Give the preparation type.
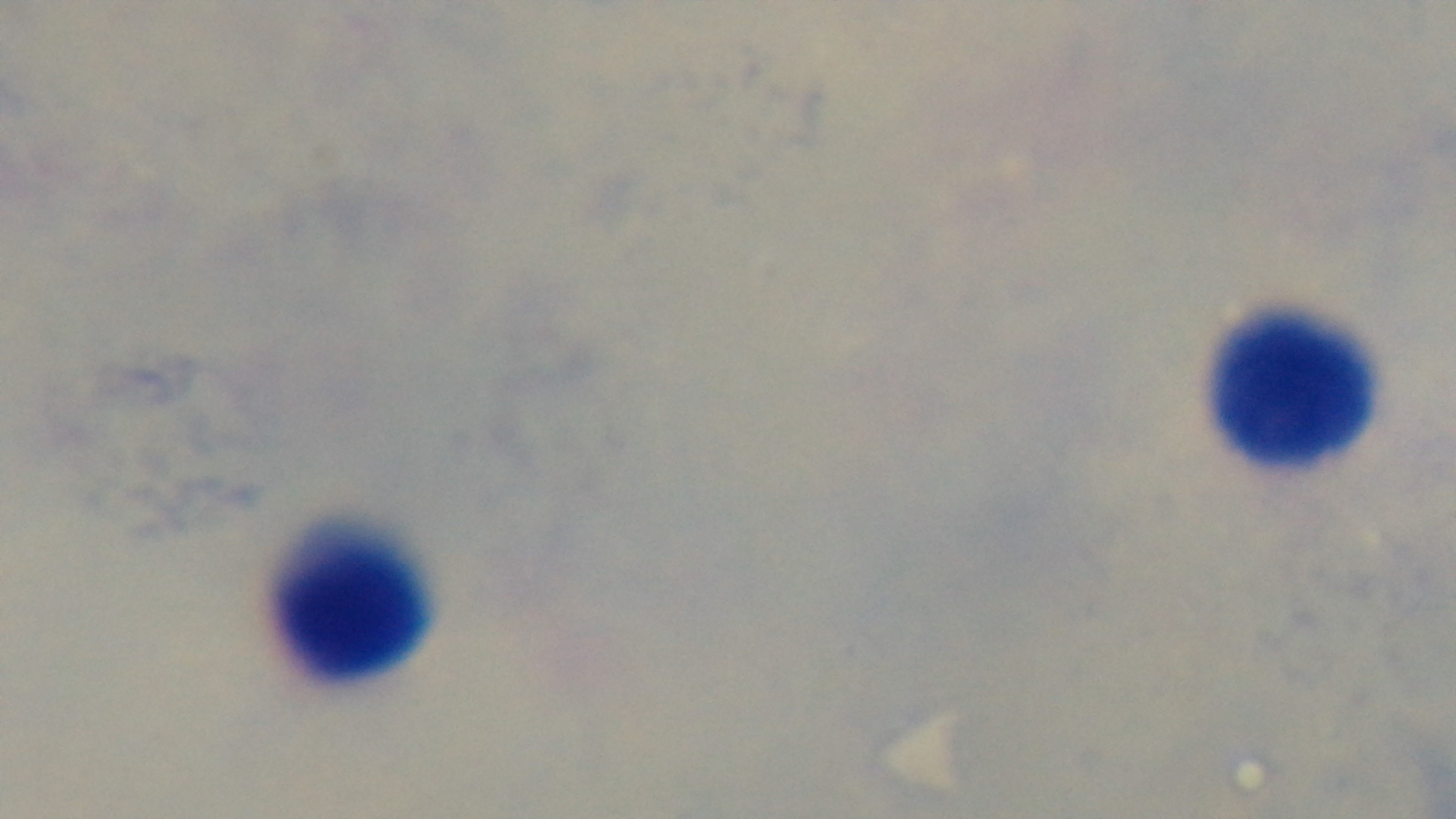
A thick smear.

Photomicrograph. Malaria status: negative. Giemsa-stained. Single field of view. 100x oil-immersion objective. Mounted 4K digital camera.